Name the cell type shown.
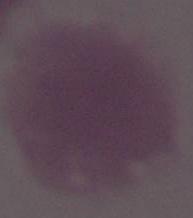

An erythrocyte.

Summary:
  - Modality: micrograph
  - Magnification: 1000x